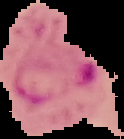

Summary:
  - Image type: cell region segmented out of the field of view; surrounding area masked to black
  - Preparation: thin blood film
  - Image size: 124×139 pixels
  - Malaria status: parasitized